Report the malaria status of this cell.
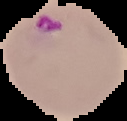

It is parasitized.

image size = 127×121 pixels
preparation = thin blood smear
image type = segmented cell region on a black background